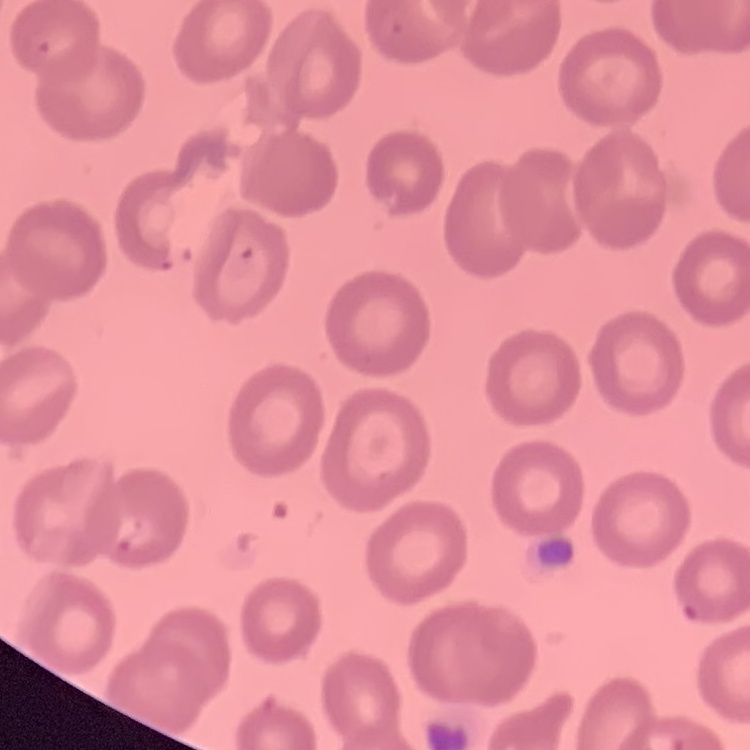

Summary:
  - Erythrocyte morphology: no rouleaux formation
  - Image type: one tile cut from a larger photomicrograph
  - Stain: Field's or Giemsa
  - Preparation: thin blood film